Report the malaria status of this cell.
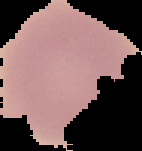
It is uninfected.

preparation = thin blood smear
image size = 142×151 pixels
image type = segmented cell region on a black background